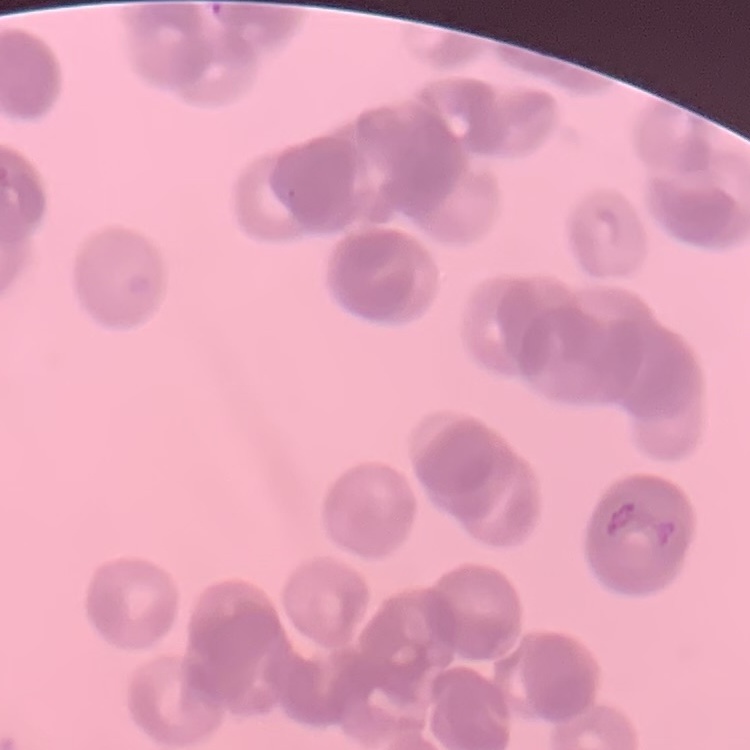
Summary:
  - Red blood cell morphology: rouleaux formation
  - Preparation: thin peripheral smear
  - Image type: square crop of a larger photomicrograph
  - Stain: Field's or Giemsa